Give the preparation type.
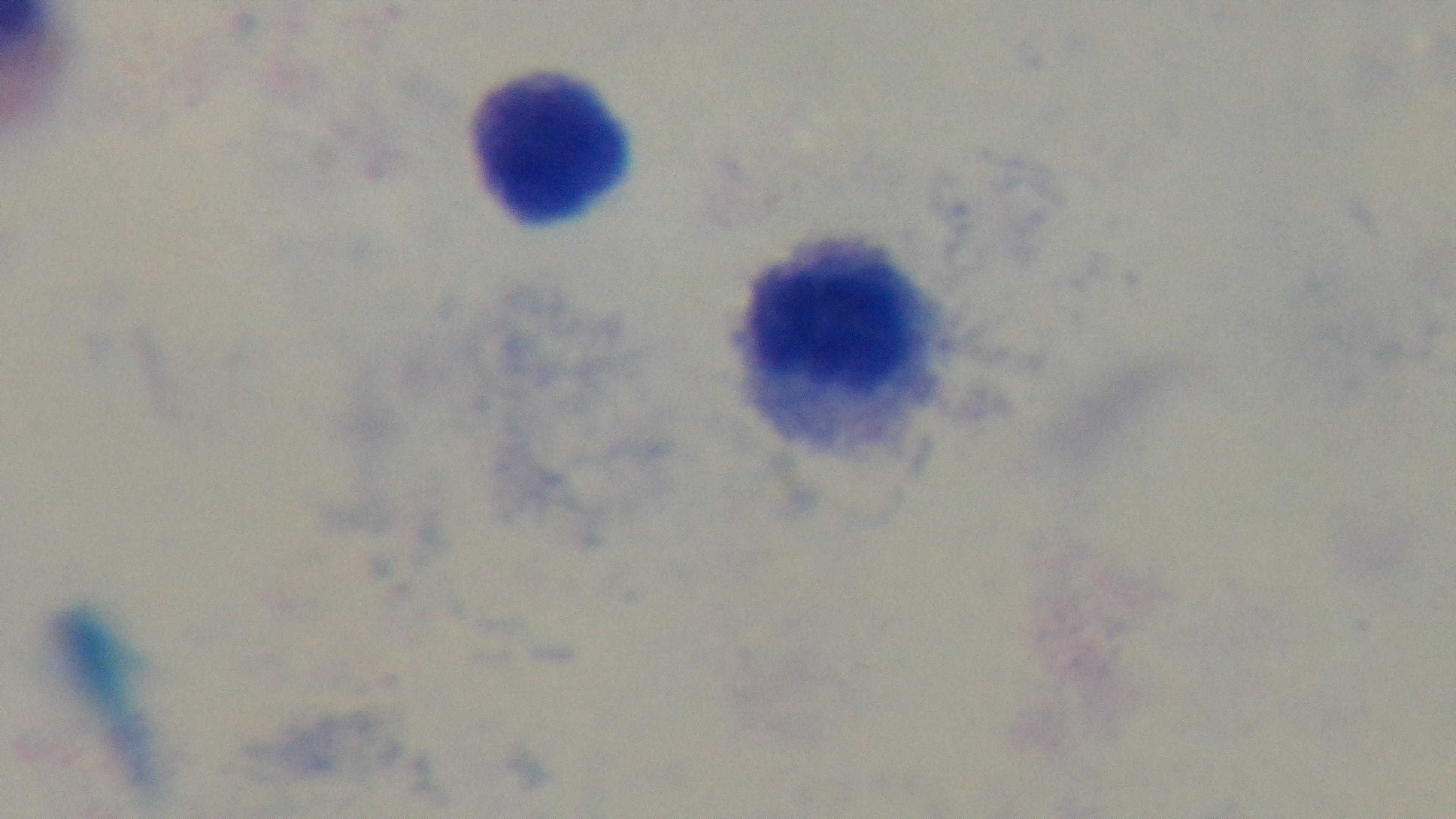

Thick.

objective: 100x oil immersion
field_of_view: single
malaria_status: uninfected
modality: light microscopy
capture: mounted 4K digital camera
stain: Giemsa